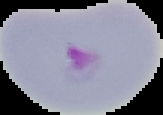
malaria status = parasitized
image size = 163×115 pixels
preparation = thin blood smear
image type = segmented cell region on a black background